Comment on the morphology of the red blood cells.
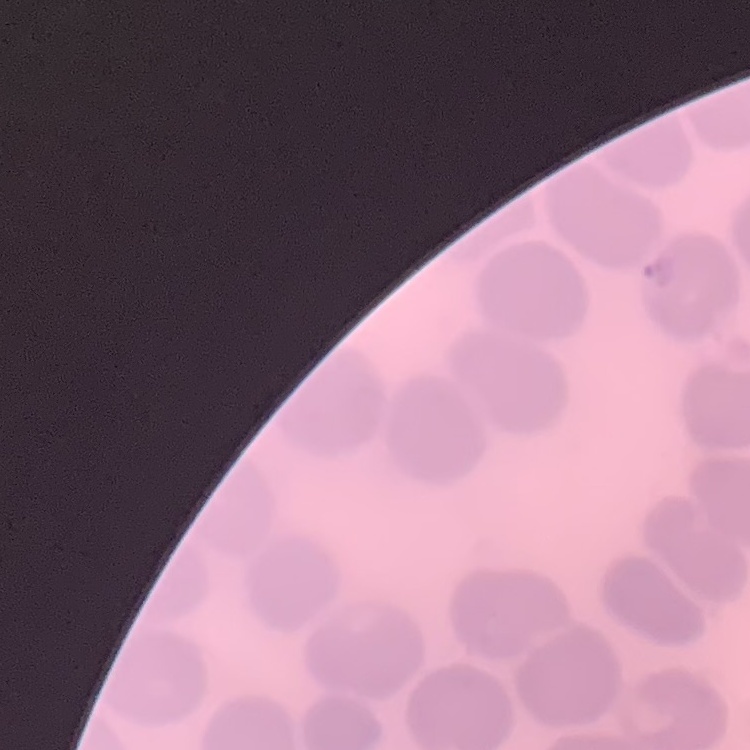
No rouleaux formation.

Summary:
  - Image type: square crop of a larger photomicrograph
  - Stain: Field's or Giemsa
  - Preparation: thin blood smear